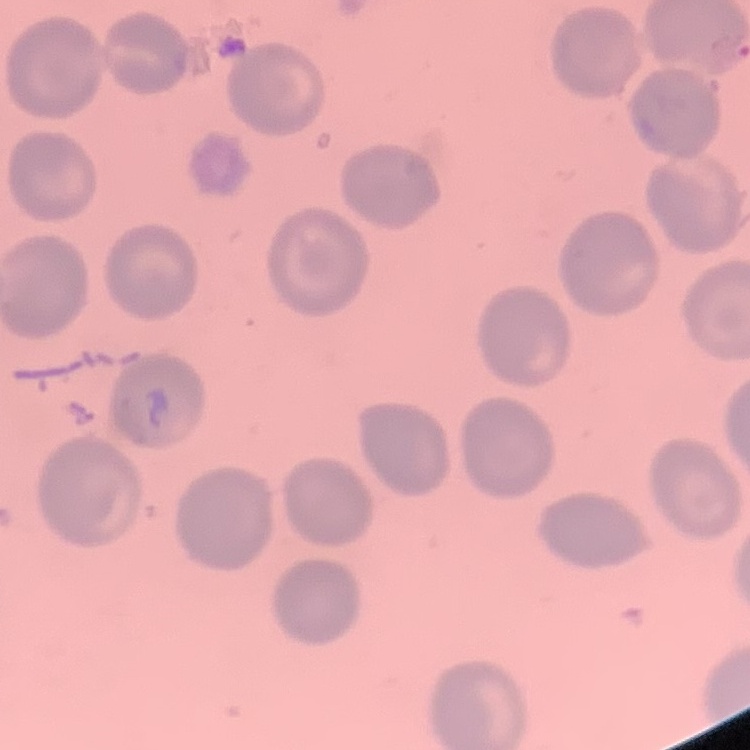

{
  "red_blood_cell_morphology": "no rouleaux formation",
  "image_type": "square crop of a larger photomicrograph",
  "stain": "Field's or Giemsa",
  "preparation": "thin blood smear"
}